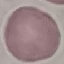
Summary:
  - Malaria status: uninfected
  - Capture: smartphone camera at the microscope eyepiece
  - Image type: cell patch, automatically extracted from a larger field of view and resized to 64 × 64 pixels
  - Stain: Giemsa
  - Preparation: thin smear